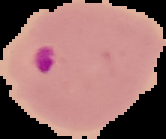

{
  "result": "Plasmodium parasites identified",
  "preparation": "thin blood film",
  "image_size": "166×139 pixels",
  "image_type": "segmented cell region with the area outside set to black"
}